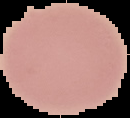
malaria status = uninfected
image size = 130×118 pixels
preparation = thin blood film
image type = cell region segmented out of the field of view; surrounding area masked to black